Comment on the morphology of the red blood cells.
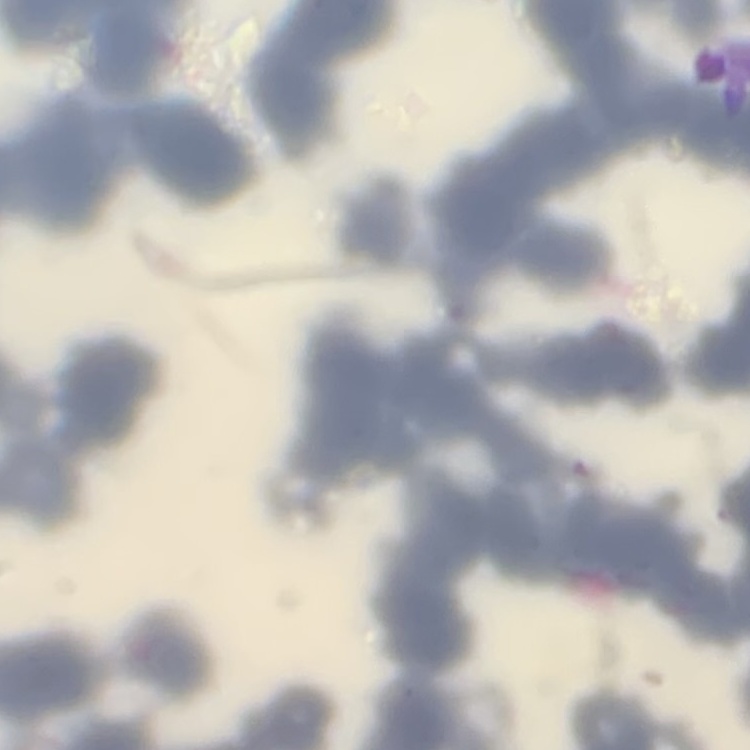

They show rouleaux formation.

Summary:
  - Stain: Field's or Giemsa
  - Image type: one tile cut from a larger photomicrograph
  - Preparation: thin blood film